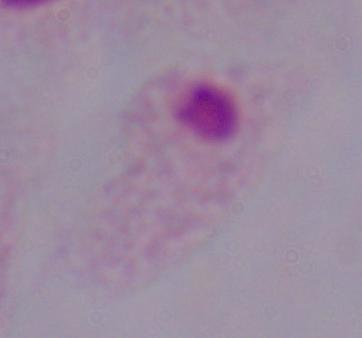

identification = trichomonad
modality = photomicrograph
magnification = 1000x